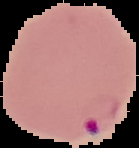
Summary:
  - Image type: cell region segmented out of the field of view; surrounding area masked to black
  - Result: Plasmodium parasites detected
  - Image size: 139×148 pixels
  - Preparation: thin blood film